Report the malaria status of this cell.
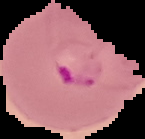

It is parasitized.

preparation = thin blood film
image type = segmented cell region on a black background
image size = 145×139 pixels